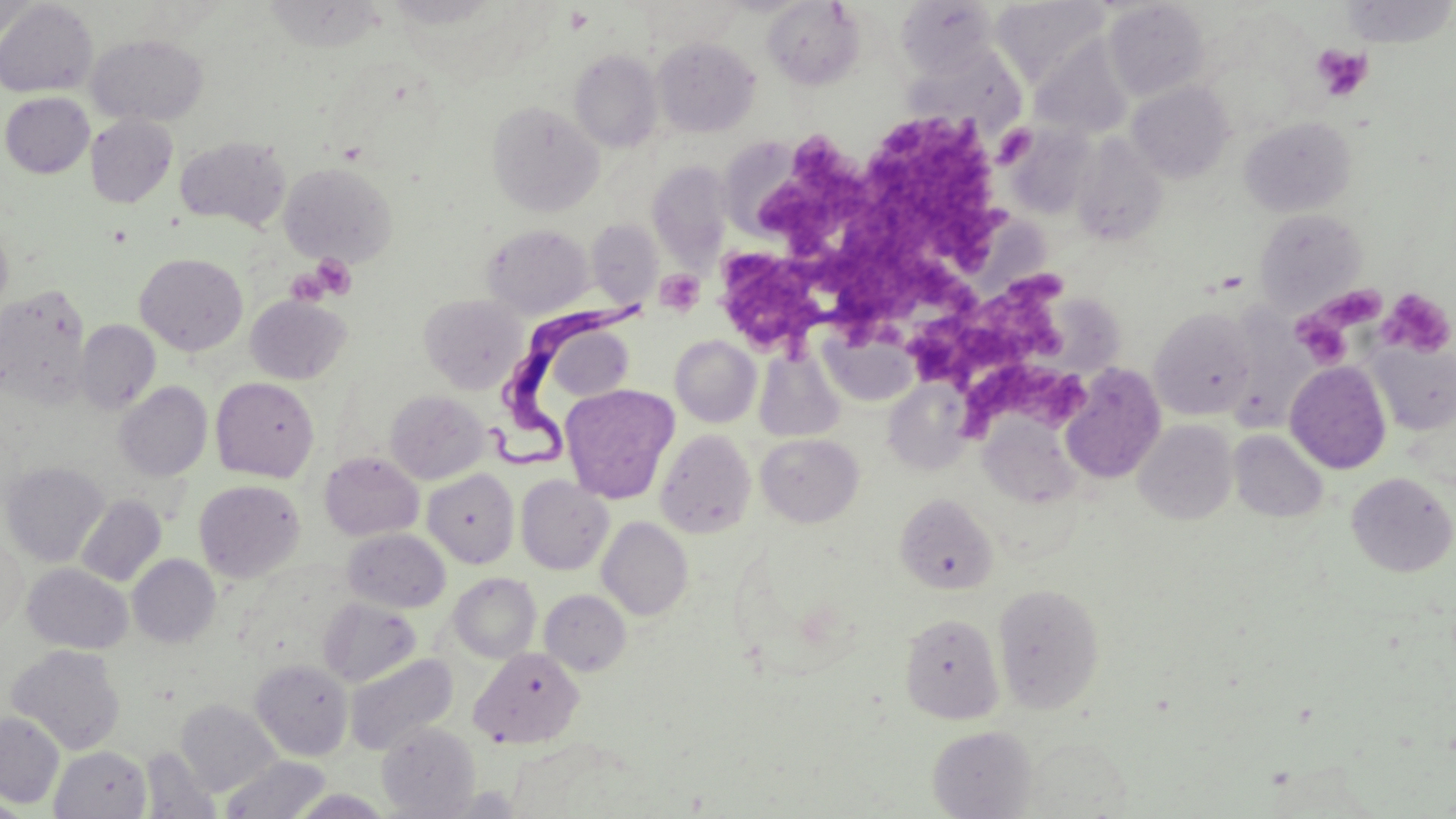
Approximate bounding boxes as [x1, y1, x2, y2] in pixels. Trypanosoma brucei locations: [492, 298, 650, 471]. Platelet locations: [563, 6, 595, 35], [1312, 45, 1372, 102], [866, 122, 1009, 273], [995, 124, 1036, 166], [757, 136, 871, 250], [822, 227, 980, 340], [719, 239, 826, 353], [312, 254, 357, 300], [284, 266, 332, 307], [654, 269, 705, 316], [901, 274, 1067, 383], [1313, 283, 1387, 332], [1377, 288, 1455, 359], [1293, 312, 1353, 368], [959, 360, 1093, 448]. Uninfected red blood cell locations: [262, 0, 385, 52], [384, 0, 499, 29], [992, 0, 1108, 83], [0, 1, 98, 97], [0, 1, 39, 42], [636, 1, 747, 51], [761, 1, 865, 91], [894, 1, 999, 77], [1104, 1, 1210, 99], [1340, 1, 1455, 47], [87, 34, 209, 126], [653, 37, 760, 137], [1032, 38, 1133, 140], [910, 46, 1025, 138], [569, 50, 663, 152], [1126, 81, 1235, 183], [1, 92, 94, 177], [487, 100, 603, 215], [85, 114, 177, 208], [1239, 117, 1356, 217], [1008, 124, 1097, 220], [1070, 133, 1168, 246], [174, 136, 291, 231], [647, 161, 734, 266], [279, 162, 398, 267], [1253, 208, 1367, 313], [0, 219, 13, 319], [587, 219, 662, 308], [483, 224, 592, 318], [135, 252, 248, 356], [0, 285, 91, 407], [419, 294, 527, 394], [245, 295, 351, 385], [1150, 307, 1257, 419], [75, 319, 160, 414], [821, 327, 916, 407], [555, 329, 637, 404], [670, 335, 761, 427], [1370, 343, 1456, 434], [754, 346, 846, 442], [1285, 361, 1392, 474], [1059, 363, 1166, 484], [210, 377, 320, 482], [883, 381, 975, 475], [114, 382, 212, 481], [561, 383, 680, 504], [385, 390, 489, 484], [979, 414, 1085, 509], [1133, 419, 1238, 524], [656, 429, 756, 539], [1229, 430, 1328, 523], [756, 433, 863, 527], [320, 452, 423, 541], [1, 461, 108, 566], [422, 468, 518, 567], [1345, 472, 1455, 577], [515, 475, 613, 575], [194, 480, 305, 583], [895, 493, 997, 594], [76, 495, 166, 587], [597, 517, 693, 620], [342, 529, 450, 613], [0, 536, 27, 633], [128, 554, 220, 647], [22, 564, 132, 654], [449, 573, 541, 662], [992, 583, 1106, 714], [540, 590, 632, 676], [319, 597, 420, 686], [899, 612, 1004, 724], [6, 645, 126, 755], [470, 647, 584, 749], [344, 653, 458, 756], [250, 659, 353, 761], [176, 699, 280, 797], [0, 712, 65, 809], [377, 722, 480, 817], [927, 725, 1036, 818], [50, 745, 152, 818], [140, 746, 221, 819], [222, 755, 329, 818], [1, 789, 30, 819]. Slide-level diagnosis: Trypanosoma brucei. Image is 1456×819 pixels. Single field of view. Thin blood smear. Optical microscopy. May-Grünwald-Giemsa stain. 1000x magnification.